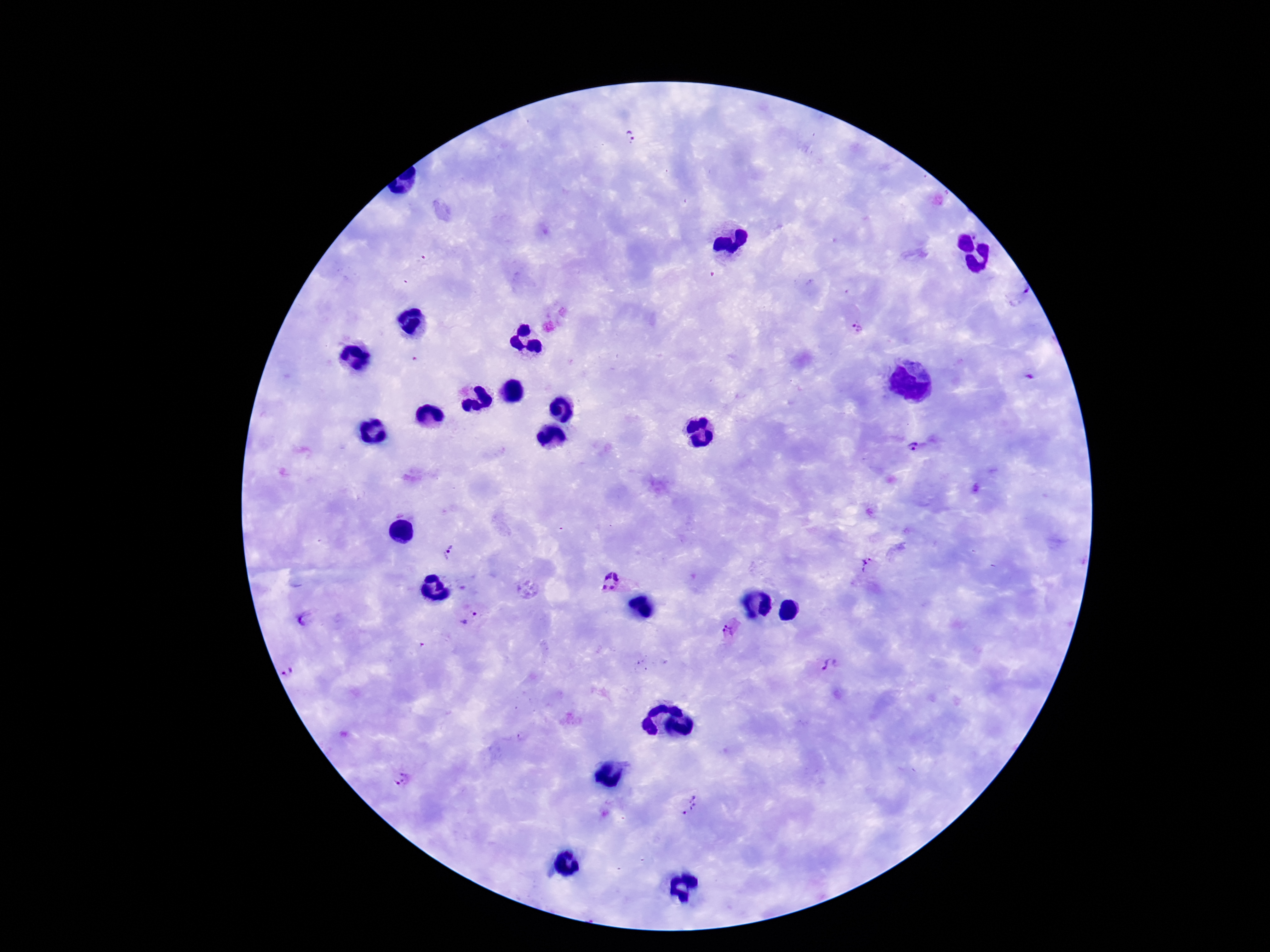 Approximate centers as [x, y] in pixels. Plasmodium parasite locations: [629, 136], [1022, 292], [858, 328], [911, 445], [448, 552], [866, 566], [612, 580], [305, 618], [470, 620], [729, 629], [829, 665], [287, 672], [402, 778], [689, 806]. Image is 1270×952 pixels. One field from this slide. Thick peripheral-blood smear. Patient malaria status: infected. 100x magnification. Smartphone photograph taken through the microscope eyepiece. Giemsa-stained preparation.